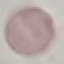
malaria status = uninfected
capture = smartphone through the microscope eyepiece
stain = Giemsa
image type = cell patch, automatically extracted from a larger field of view and resized to 64 × 64 pixels
preparation = thin blood smear